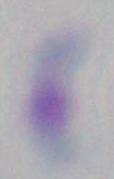

Summary:
  - Magnification: 1000x
  - Identification: Toxoplasma gondii
  - Modality: micrograph